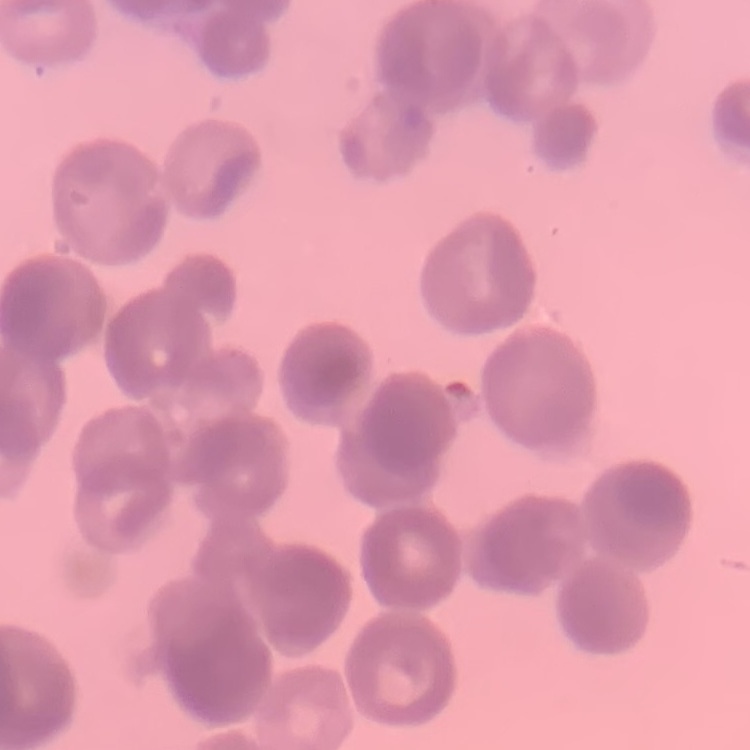

The erythrocytes show rouleaux formation. Field's or Giemsa stain. Square crop of a larger photomicrograph. Thin blood smear.